Name the parasite shown.
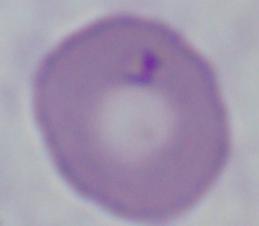

Babesia.

modality: photomicrograph
magnification: 1000x